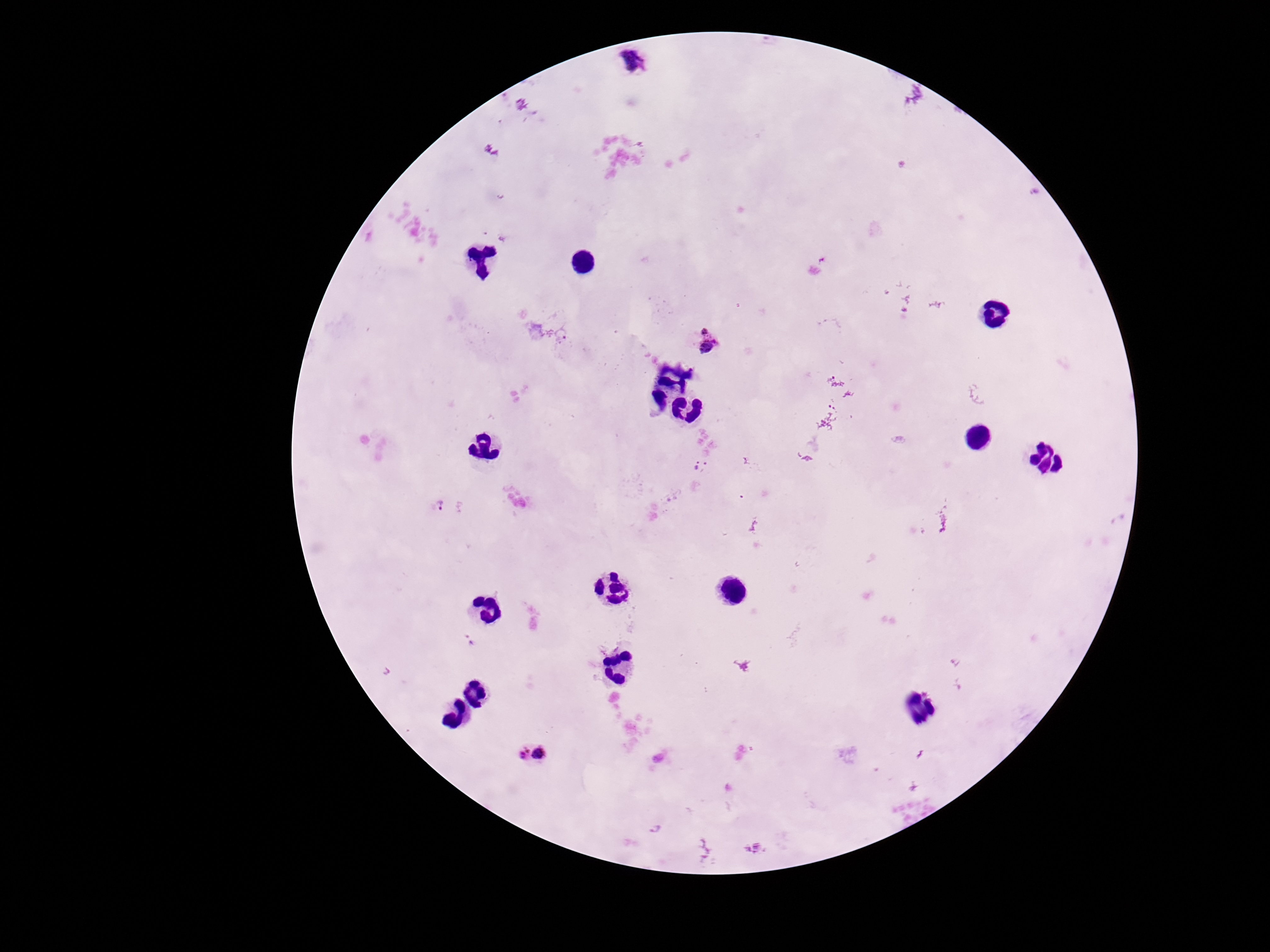
patient malaria status = infected
field of view = one from this slide
image size = 1270×952 pixels
Plasmodium parasite locations = approximate centers as (x, y) in pixels: (636, 64), (560, 334), (708, 341), (701, 466), (440, 507), (469, 641), (535, 755), (655, 830)
capture = smartphone camera through the microscope eyepiece
stain = Giemsa
magnification = 100x
preparation = thick blood film